Locate every Plasmodium parasite.
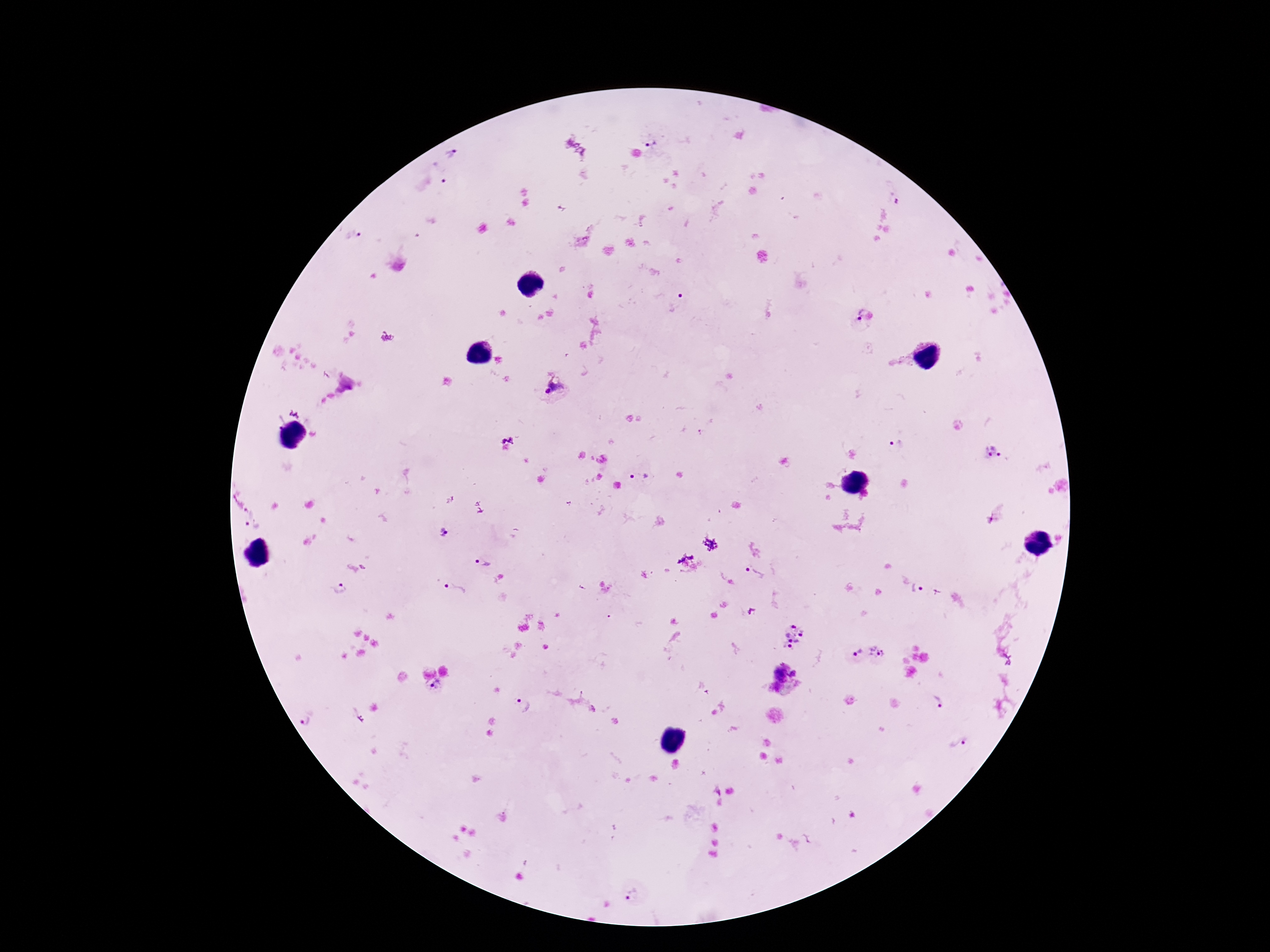

Approximate centers as {x, y} in pixels.
Plasmodium parasites: {653, 145}, {455, 152}, {438, 170}, {893, 195}, {355, 236}, {678, 302}, {864, 320}, {555, 387}, {898, 445}, {992, 452}, {641, 476}, {250, 509}, {250, 530}, {445, 532}, {483, 564}, {756, 574}, {455, 589}, {918, 590}, {341, 591}, {794, 636}, {855, 652}, {876, 652}, {794, 673}, {780, 674}, {434, 689}, {520, 704}, {939, 705}, {305, 722}, {634, 896}.

magnification: 100x
field_of_view: single
stain: Giemsa
image_size: 1270×952 pixels
capture: smartphone camera through the microscope eyepiece
preparation: thick blood film
patient_malaria_status: infected